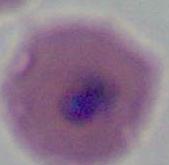

Summary:
  - Identification: Plasmodium
  - Modality: photomicrograph
  - Magnification: 400x or 1000x